Classify this cell by malaria status.
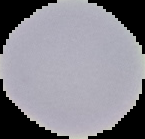
It is uninfected.

Summary:
  - Image size: 145×139 pixels
  - Preparation: thin blood film
  - Image type: cell region segmented out of the field of view; surrounding area masked to black